Report the malaria status of this cell.
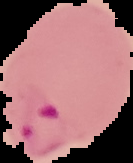

Parasitized.

Summary:
  - Image type: segmented cell region on a black background
  - Preparation: thin blood smear
  - Image size: 133×163 pixels